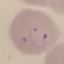

result = malaria parasites detected
preparation = thin blood film
image type = cell patch, automatically extracted from a larger field of view and resized to 64 × 64 pixels
stain = Giemsa
capture = smartphone camera at the microscope eyepiece